Comment on the morphology of the red blood cells.
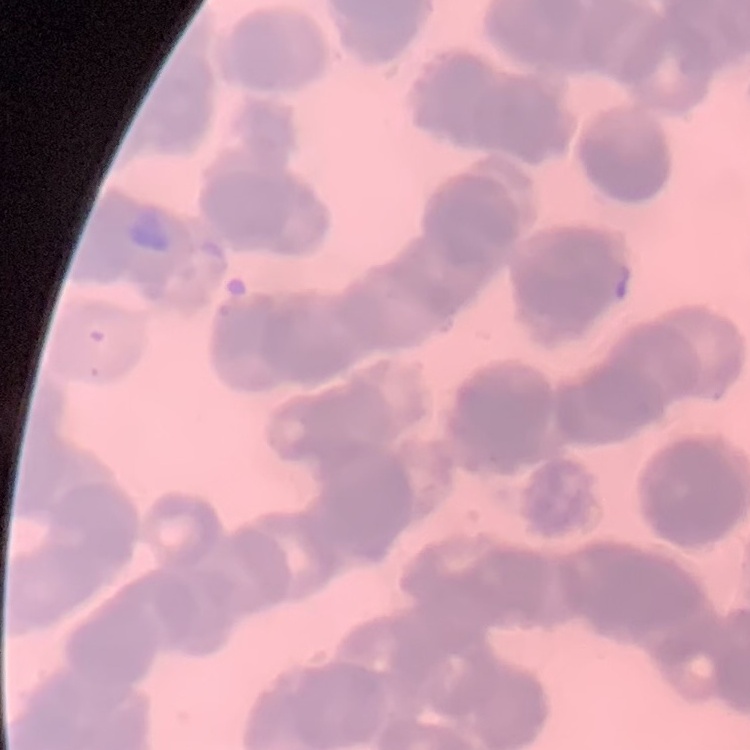
Rouleaux formation.

Thin blood smear. Field's or Giemsa stain. Square crop of a larger photomicrograph.